Identify the preparation type.
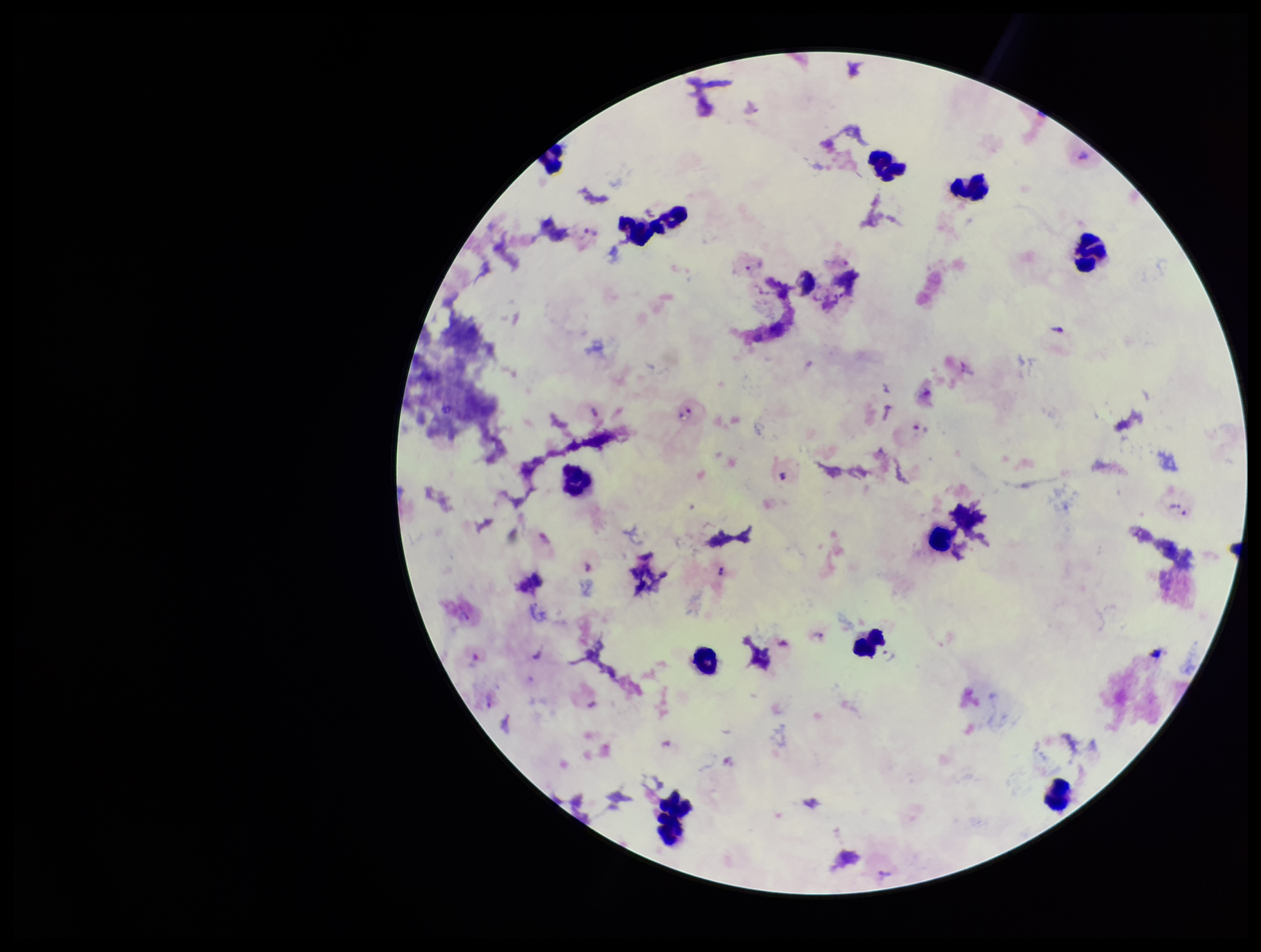

It is a thick blood smear.

Single field of view. Patient malaria status: infected. Parasite count: 16. Leukocyte count: 14. Image is 1261×952 pixels. Species reported for this patient: Plasmodium vivax. Plasmodium parasites: identified. Giemsa stain. Photographed through the microscope eyepiece with a smartphone camera.